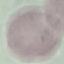 Malaria status: uninfected. Giemsa stain. Acquired by smartphone through the microscope eyepiece. Thin smear of blood. Automatically extracted cell patch, resized to 64 × 64 pixels.